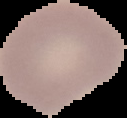
Summary:
  - Malaria status: uninfected
  - Image size: 127×118 pixels
  - Image type: segmented cell region with the area outside set to black
  - Preparation: thin blood smear